Look for Plasmodium parasites.
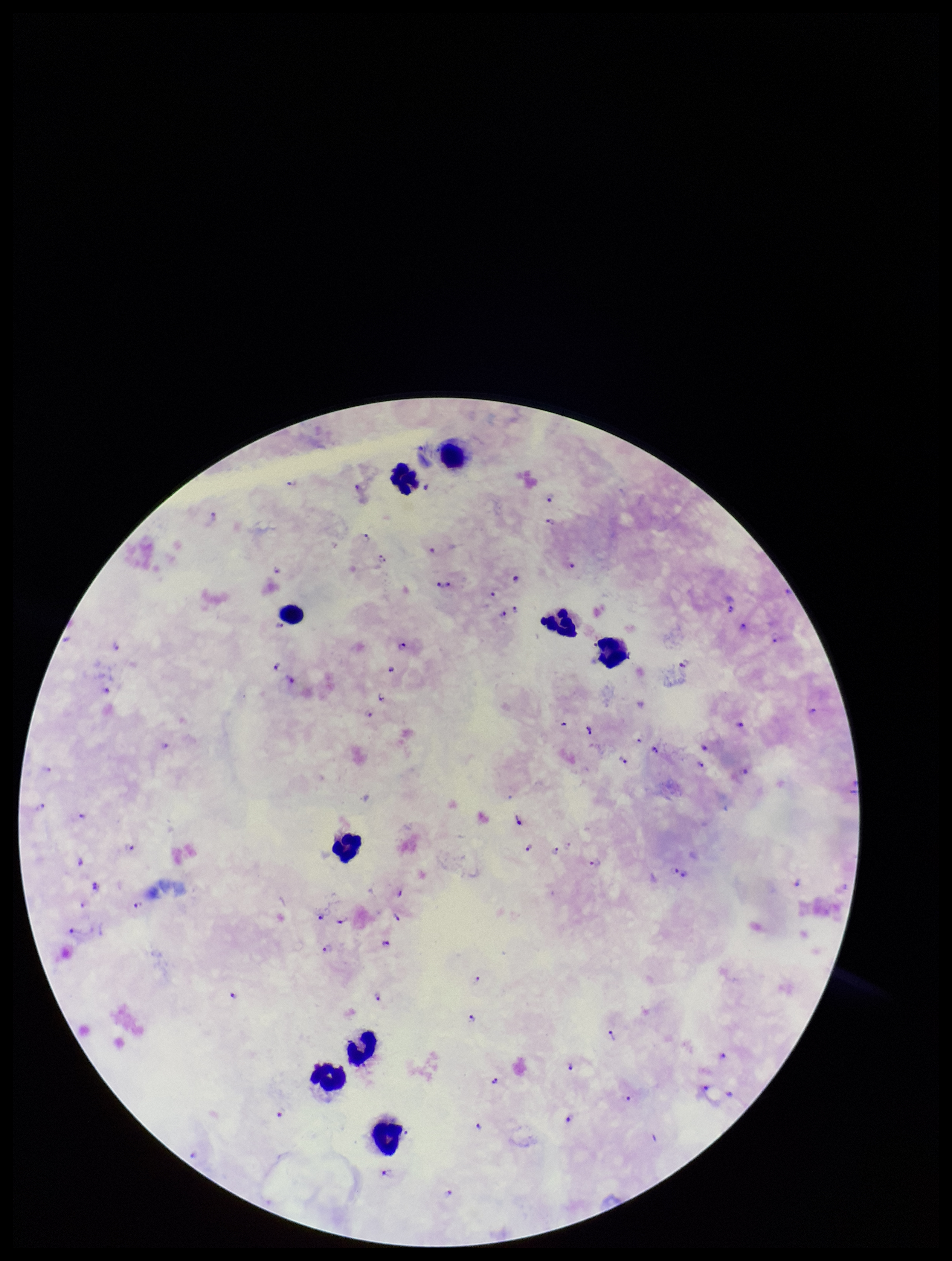

Identified.

Summary:
  - Parasite count: 60
  - Preparation: thick
  - Species reported for this patient: Plasmodium falciparum
  - Capture: smartphone photograph through the microscope eyepiece
  - Field of view: one from this slide
  - Patient malaria status: positive
  - Image size: 952×1261 pixels
  - Stain: Giemsa
  - Leukocyte count: 9